State which parasite is depicted.
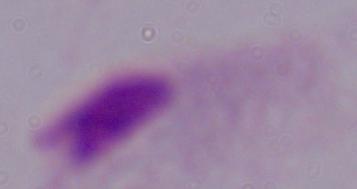

A trichomonad.

{
  "modality": "micrograph",
  "magnification": "1000x"
}